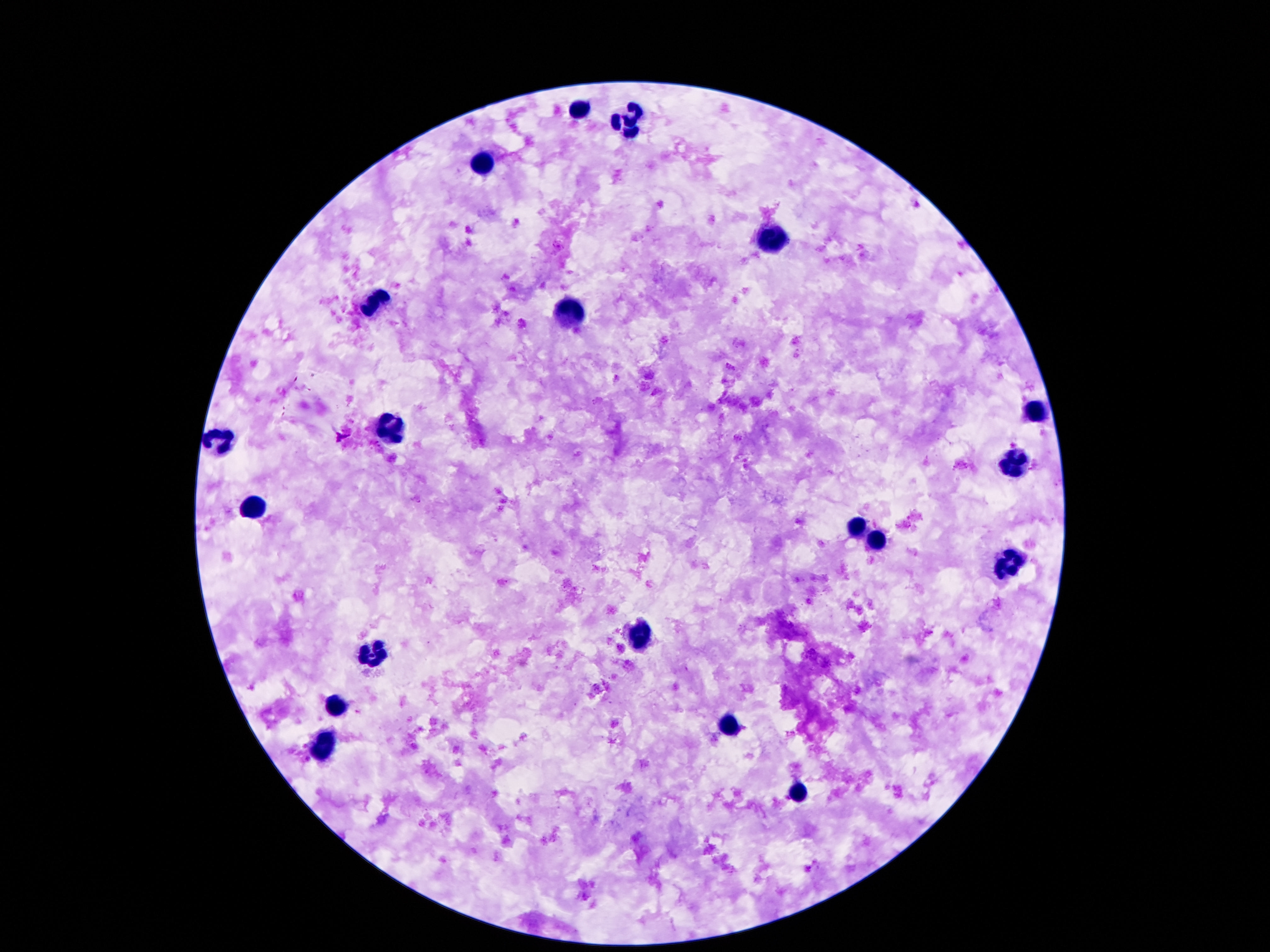
Approximate centers as {x, y} in pixels. Leukocyte locations: {582, 108}, {630, 121}, {482, 164}, {776, 237}, {376, 299}, {571, 310}, {1035, 409}, {392, 432}, {220, 438}, {1013, 463}, {257, 508}, {858, 530}, {876, 542}, {1011, 564}, {641, 637}, {376, 652}, {336, 709}, {728, 728}, {325, 742}, {801, 797}. Image is 1270×952 pixels. One field from this slide. Patient malaria status: not infected. Giemsa-stained preparation. 100x magnification. Smartphone photograph taken through the microscope eyepiece. Thick blood smear.